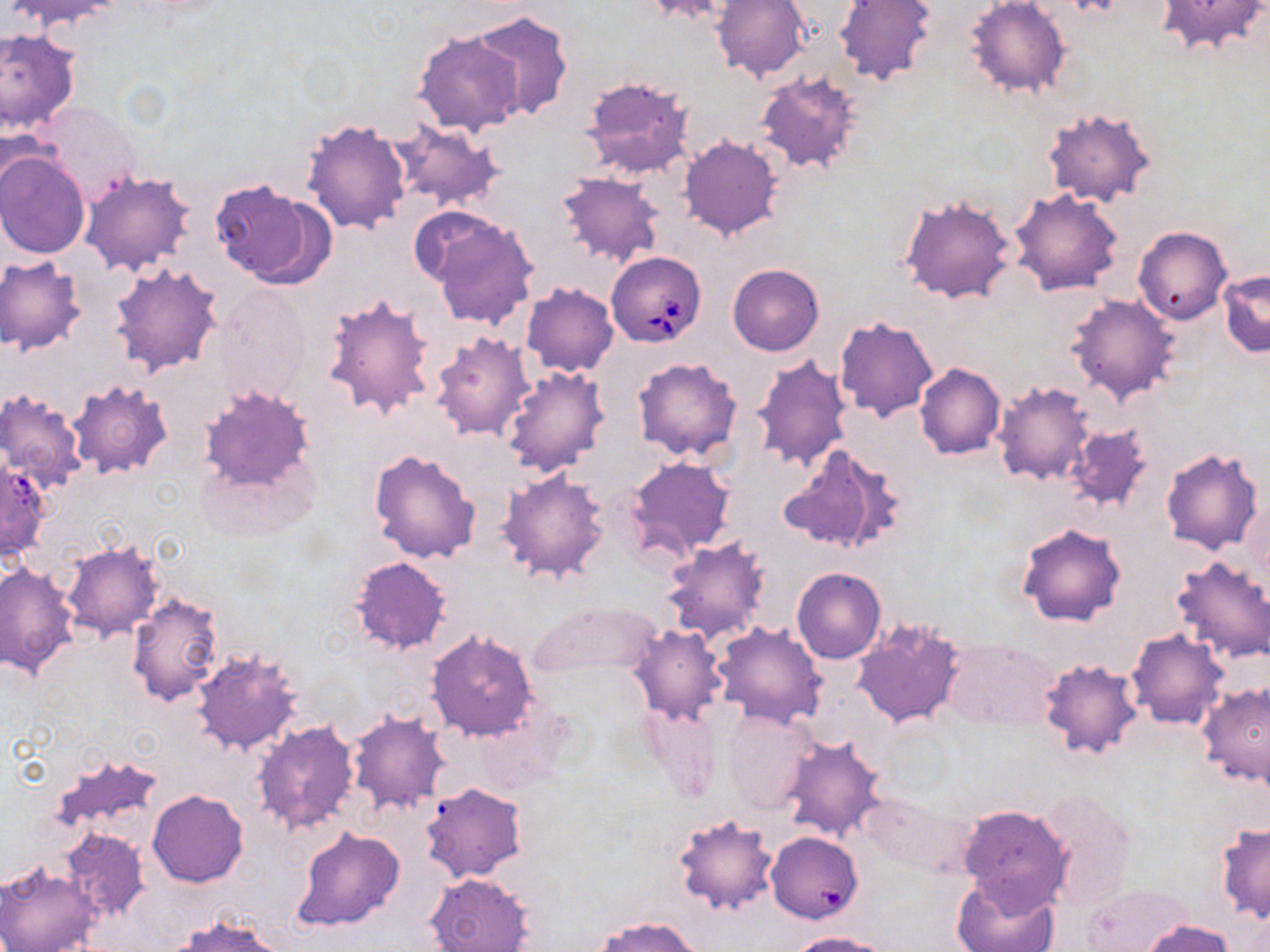 Approximate bounding boxes as (x1, y1, x2, y2) in pixels. Babesia divergens-infected red blood cell locations: (605, 251, 706, 347). Uninfected red blood cell locations: (6, 0, 124, 34), (642, 0, 736, 25), (711, 0, 809, 82), (965, 0, 1071, 100), (1154, 0, 1267, 57), (833, 1, 937, 87), (467, 9, 573, 121), (0, 28, 79, 137), (414, 30, 527, 136), (754, 70, 864, 175), (579, 76, 697, 179), (1042, 107, 1158, 208), (302, 118, 411, 237), (389, 120, 505, 212), (678, 135, 783, 241), (0, 149, 89, 258), (81, 169, 195, 277), (556, 172, 665, 267), (210, 176, 334, 288), (1009, 188, 1125, 296), (898, 191, 1018, 304), (421, 211, 539, 331), (1133, 226, 1232, 324), (0, 256, 87, 355), (110, 262, 224, 377), (727, 264, 823, 356), (1219, 270, 1270, 357), (521, 282, 618, 376), (215, 286, 311, 407), (1066, 292, 1181, 405), (321, 294, 439, 421), (834, 314, 939, 422), (430, 332, 537, 441), (751, 354, 853, 473), (632, 357, 741, 462), (914, 362, 1005, 459), (501, 366, 609, 477), (67, 379, 174, 478), (991, 380, 1096, 487), (197, 383, 318, 509), (0, 389, 87, 489), (1066, 424, 1153, 514), (778, 444, 903, 556), (1160, 445, 1265, 556), (368, 447, 481, 564), (624, 455, 737, 561), (0, 456, 49, 560), (497, 467, 610, 585), (1015, 521, 1127, 628), (660, 536, 772, 644), (59, 540, 165, 641), (0, 552, 155, 664), (1170, 555, 1269, 665), (348, 556, 453, 655), (0, 561, 81, 683), (791, 566, 886, 663), (127, 593, 224, 706), (821, 597, 933, 705), (527, 600, 662, 679), (851, 618, 967, 729), (712, 620, 828, 730), (627, 624, 727, 726), (1127, 628, 1229, 730), (424, 629, 539, 742), (942, 636, 1057, 730), (190, 649, 304, 757), (1038, 656, 1144, 761), (1196, 682, 1270, 788), (639, 698, 724, 803), (722, 708, 817, 815), (347, 711, 450, 815), (251, 719, 360, 837), (779, 733, 888, 842), (43, 751, 165, 849), (421, 783, 526, 883), (147, 789, 248, 886), (1033, 790, 1138, 912), (859, 792, 970, 874), (958, 803, 1072, 910), (672, 812, 779, 918), (1215, 822, 1270, 923), (291, 827, 406, 933), (58, 829, 149, 924), (766, 832, 863, 923), (0, 862, 102, 952), (426, 872, 533, 952), (951, 872, 1060, 952), (1081, 883, 1195, 951), (169, 913, 286, 952), (593, 915, 703, 952), (1136, 918, 1235, 952), (787, 931, 888, 952). Platelet locations: (1065, 0, 1126, 20). Slide-level diagnosis: Babesia divergens. May-Grünwald-Giemsa stain. Image is 1270×952 pixels. Light microscopy. Thin blood film. One field of a larger specimen. 1000x magnification.